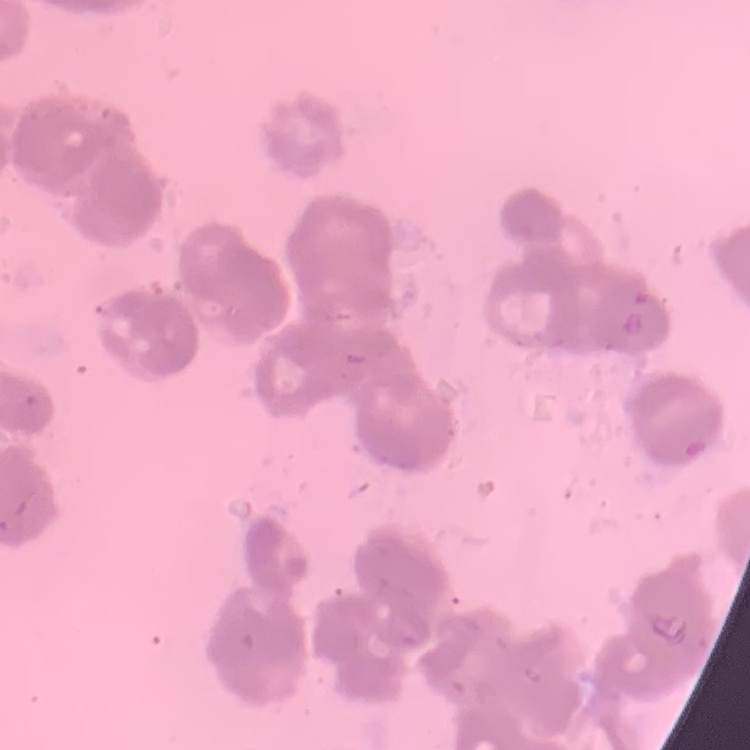

Summary:
  - Red blood cell morphology: rouleaux formation
  - Image type: one tile cut from a larger photomicrograph
  - Preparation: thin blood film
  - Stain: Field's or Giemsa